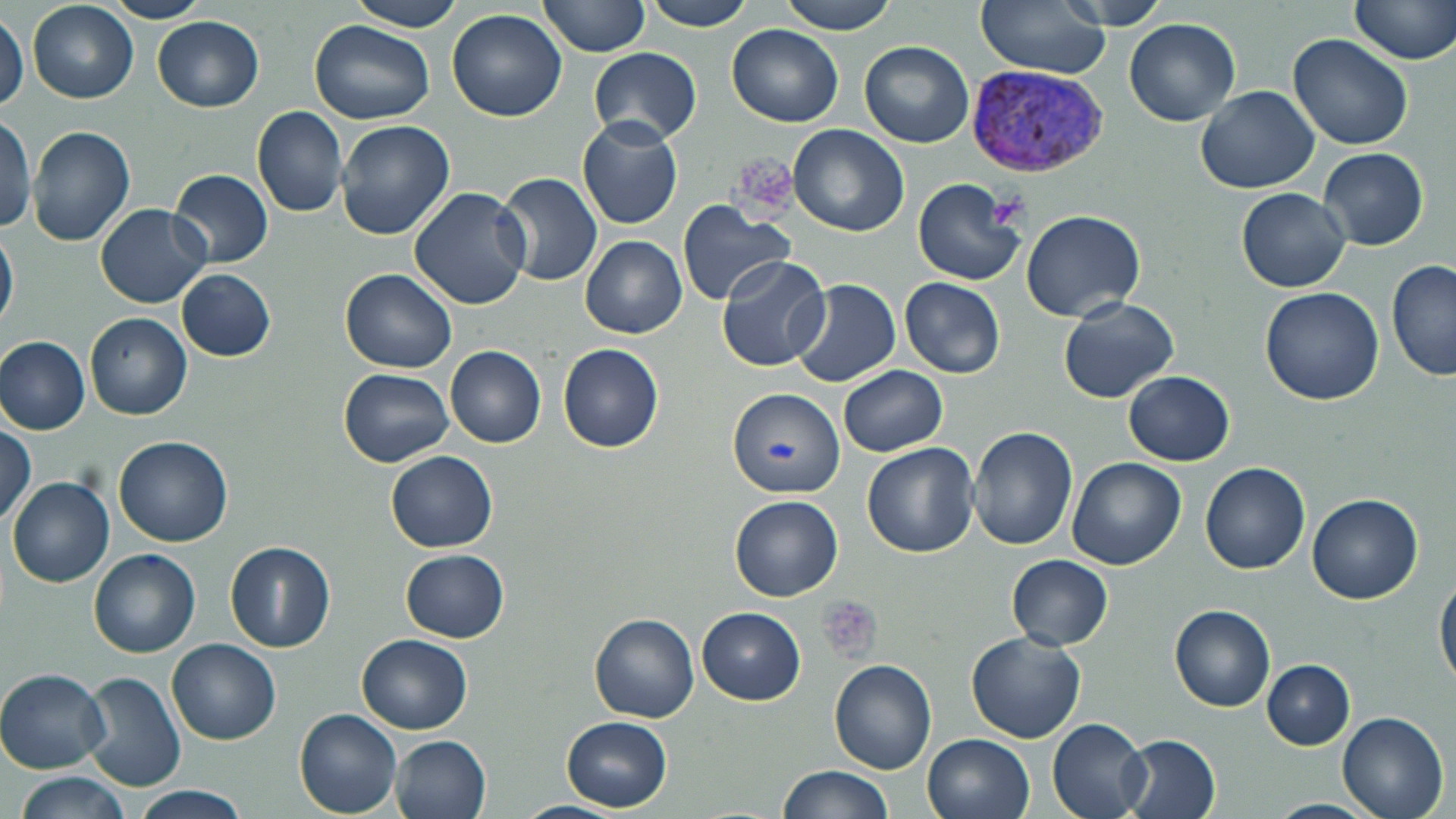
slide-level diagnosis = Plasmodium vivax
stain = May-Grünwald-Giemsa
uninfected red blood cell locations = approximate bounding boxes as named x1/y1/x2/y2 corners in pixels: (x1=103, y1=0, x2=212, y2=23), (x1=349, y1=0, x2=470, y2=31), (x1=536, y1=0, x2=650, y2=58), (x1=644, y1=0, x2=758, y2=31), (x1=780, y1=0, x2=900, y2=33), (x1=978, y1=0, x2=1107, y2=77), (x1=1054, y1=0, x2=1170, y2=31), (x1=1350, y1=0, x2=1456, y2=66), (x1=27, y1=2, x2=138, y2=104), (x1=448, y1=9, x2=567, y2=122), (x1=1, y1=14, x2=27, y2=113), (x1=152, y1=17, x2=264, y2=111), (x1=1125, y1=18, x2=1240, y2=125), (x1=309, y1=21, x2=435, y2=124), (x1=728, y1=24, x2=845, y2=127), (x1=1288, y1=33, x2=1415, y2=150), (x1=860, y1=41, x2=974, y2=146), (x1=590, y1=48, x2=702, y2=143), (x1=1196, y1=85, x2=1319, y2=193), (x1=252, y1=106, x2=348, y2=217), (x1=0, y1=114, x2=36, y2=234), (x1=577, y1=118, x2=685, y2=229), (x1=335, y1=119, x2=455, y2=241), (x1=27, y1=124, x2=136, y2=247), (x1=789, y1=124, x2=910, y2=236), (x1=1320, y1=147, x2=1429, y2=250), (x1=169, y1=168, x2=274, y2=268), (x1=496, y1=171, x2=603, y2=285), (x1=913, y1=177, x2=1028, y2=287), (x1=409, y1=187, x2=532, y2=310), (x1=1237, y1=187, x2=1351, y2=292), (x1=677, y1=199, x2=798, y2=307), (x1=95, y1=203, x2=211, y2=308), (x1=1021, y1=208, x2=1146, y2=321), (x1=0, y1=226, x2=19, y2=333), (x1=581, y1=236, x2=687, y2=338), (x1=717, y1=254, x2=834, y2=373), (x1=1387, y1=260, x2=1455, y2=383), (x1=175, y1=268, x2=277, y2=361), (x1=342, y1=269, x2=457, y2=374), (x1=899, y1=277, x2=1007, y2=378), (x1=789, y1=280, x2=901, y2=389), (x1=1259, y1=285, x2=1385, y2=406), (x1=1059, y1=296, x2=1179, y2=404), (x1=85, y1=313, x2=192, y2=419), (x1=0, y1=336, x2=90, y2=434), (x1=558, y1=343, x2=664, y2=454), (x1=445, y1=346, x2=547, y2=448), (x1=839, y1=365, x2=947, y2=456), (x1=339, y1=367, x2=454, y2=467), (x1=1124, y1=370, x2=1235, y2=465), (x1=729, y1=386, x2=843, y2=498), (x1=0, y1=421, x2=36, y2=523), (x1=968, y1=426, x2=1077, y2=549), (x1=115, y1=435, x2=234, y2=546), (x1=862, y1=443, x2=978, y2=558), (x1=387, y1=450, x2=497, y2=551), (x1=1067, y1=456, x2=1184, y2=569), (x1=1201, y1=464, x2=1310, y2=575), (x1=8, y1=476, x2=115, y2=586), (x1=730, y1=495, x2=844, y2=600), (x1=1306, y1=495, x2=1424, y2=604), (x1=226, y1=540, x2=335, y2=653), (x1=89, y1=548, x2=201, y2=658), (x1=401, y1=549, x2=508, y2=642), (x1=1008, y1=555, x2=1115, y2=650), (x1=1436, y1=574, x2=1456, y2=692), (x1=1170, y1=604, x2=1276, y2=712), (x1=698, y1=606, x2=806, y2=705), (x1=590, y1=615, x2=698, y2=722), (x1=965, y1=631, x2=1088, y2=744), (x1=358, y1=634, x2=473, y2=733), (x1=168, y1=639, x2=281, y2=744), (x1=829, y1=657, x2=936, y2=775), (x1=1263, y1=660, x2=1356, y2=750), (x1=0, y1=669, x2=111, y2=773), (x1=80, y1=671, x2=187, y2=792), (x1=295, y1=708, x2=403, y2=816), (x1=1336, y1=711, x2=1449, y2=819), (x1=562, y1=715, x2=672, y2=812), (x1=1048, y1=715, x2=1153, y2=819), (x1=923, y1=733, x2=1035, y2=819), (x1=1118, y1=733, x2=1221, y2=819), (x1=391, y1=735, x2=493, y2=819), (x1=777, y1=764, x2=895, y2=819), (x1=15, y1=771, x2=135, y2=819), (x1=131, y1=787, x2=250, y2=819), (x1=1266, y1=799, x2=1376, y2=819), (x1=514, y1=801, x2=622, y2=819)
Plasmodium vivax-infected red blood cell locations = approximate bounding boxes as named x1/y1/x2/y2 corners in pixels: (x1=964, y1=66, x2=1112, y2=178)
preparation = thin blood smear
magnification = 1000x
image size = 1456×819 pixels
platelet locations = approximate bounding boxes as named x1/y1/x2/y2 corners in pixels: (x1=732, y1=150, x2=799, y2=214), (x1=989, y1=193, x2=1028, y2=229), (x1=817, y1=595, x2=884, y2=663)
field of view = single
modality = light microscopy